Identify the blood parasite species.
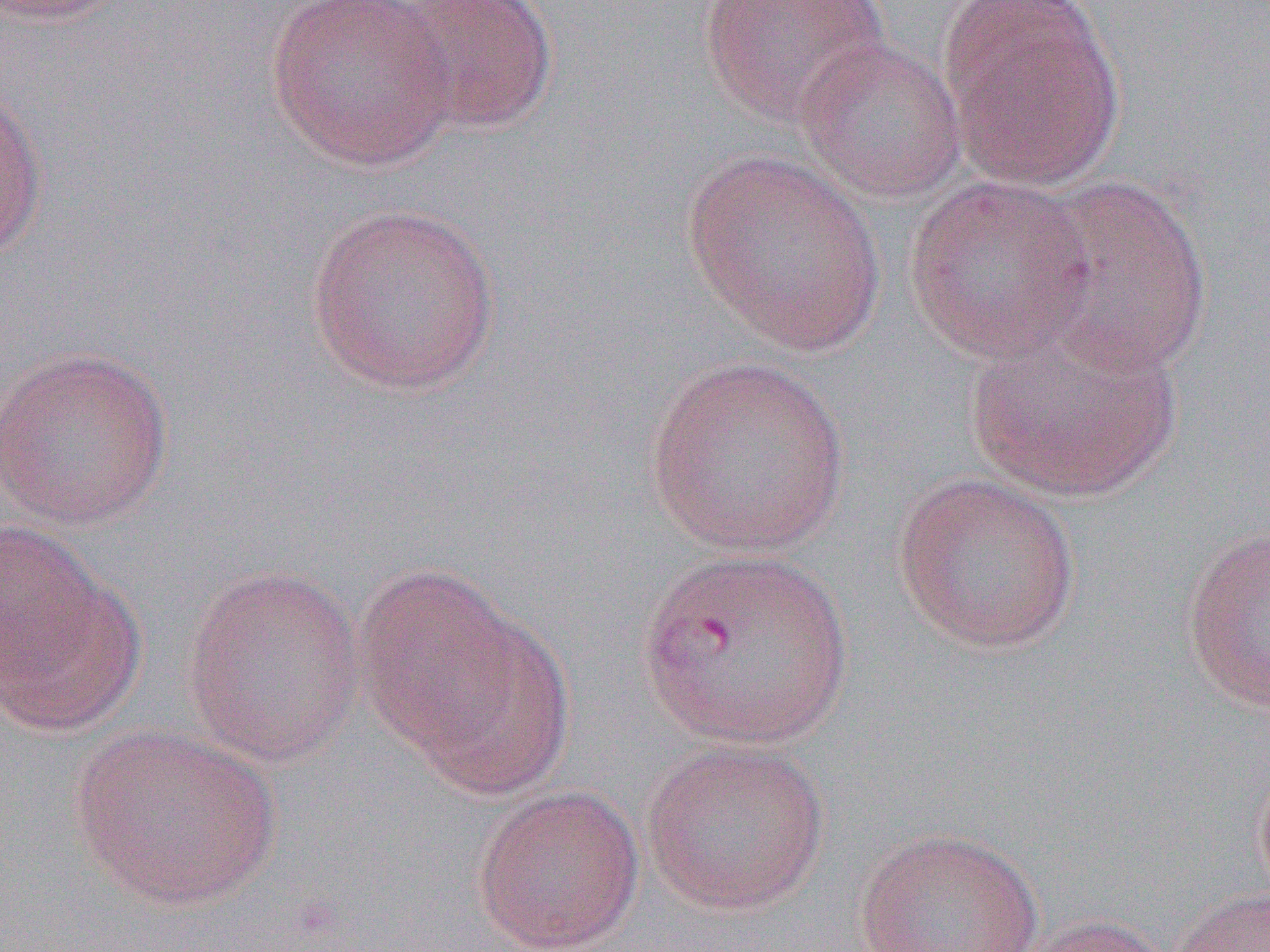

Plasmodium vivax.

image size = 1270×952 pixels
Plasmodium vivax-infected red blood cell locations = approximate bounding boxes as (x1, y1, x2, y2) in pixels: (634, 545, 854, 751)
uninfected red blood cell locations = approximate bounding boxes as (x1, y1, x2, y2) in pixels: (0, 0, 135, 27), (265, 0, 460, 172), (388, 0, 559, 136), (696, 0, 891, 128), (938, 3, 1125, 188), (794, 35, 967, 204), (0, 80, 48, 264), (682, 150, 886, 354), (903, 175, 1098, 364), (1022, 175, 1215, 378), (304, 202, 502, 395), (964, 319, 1184, 505), (0, 344, 174, 532), (644, 354, 851, 557), (891, 472, 1083, 654), (1180, 524, 1270, 716), (1, 531, 141, 733), (351, 563, 539, 764), (180, 564, 366, 767), (70, 724, 281, 911), (639, 736, 831, 916), (470, 784, 645, 952), (853, 826, 1043, 952), (1172, 886, 1270, 952), (1011, 914, 1178, 952)
modality = optical microscopy
field of view = single
magnification = 1000x
preparation = thin blood film